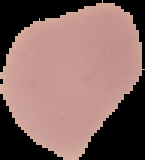

{
  "preparation": "thin blood film",
  "image_type": "segmented cell region on a black background",
  "image_size": "145×160 pixels",
  "result": "no malaria parasites seen"
}